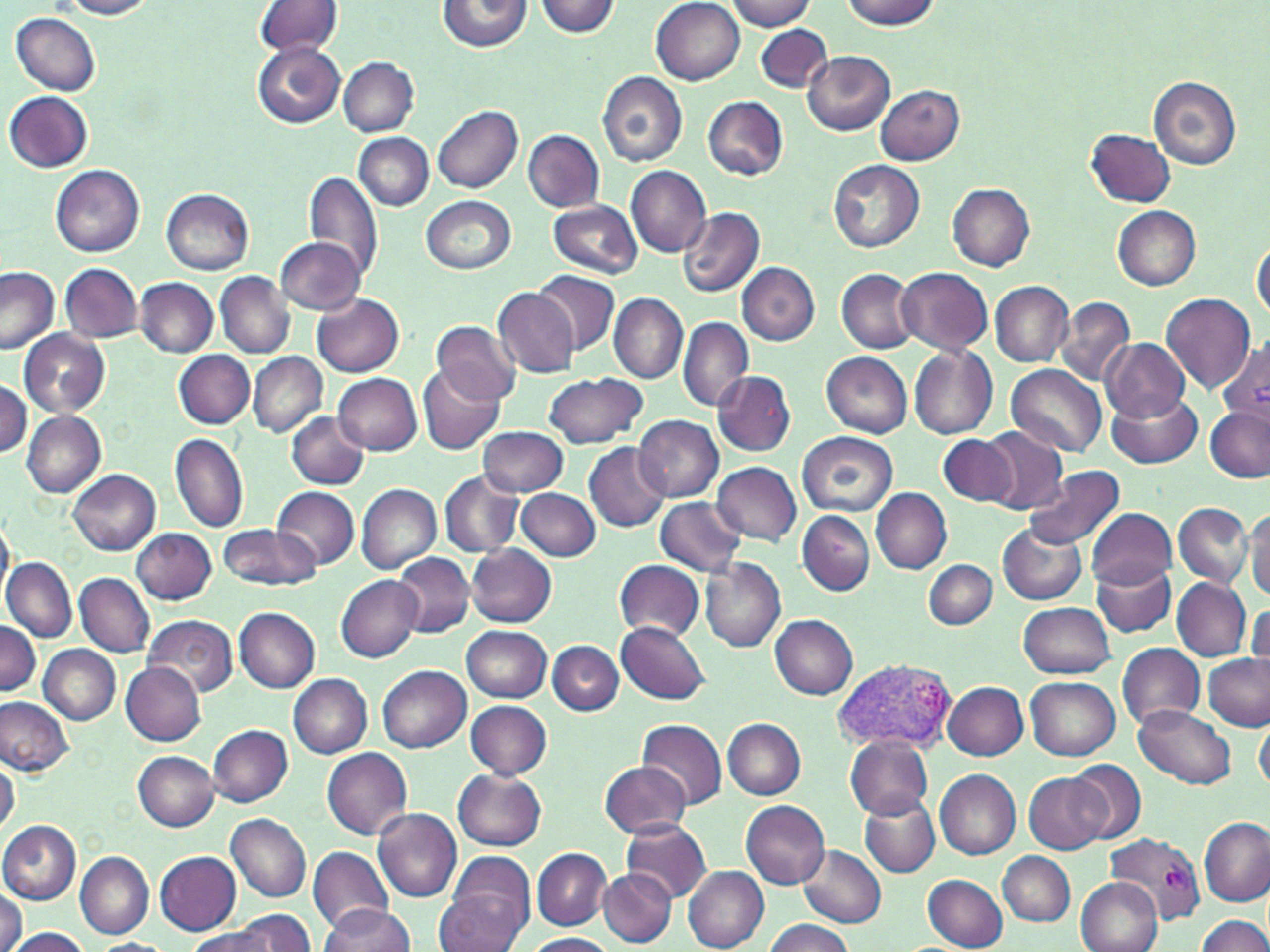

Approximate bounding boxes as (x1, y1, x2, y2) in pixels. Uninfected red blood cell locations: (56, 0, 158, 20), (724, 0, 817, 32), (253, 1, 342, 59), (436, 1, 531, 53), (534, 1, 622, 37), (651, 1, 745, 85), (839, 1, 942, 29), (11, 12, 101, 95), (756, 26, 832, 92), (251, 39, 345, 129), (803, 52, 895, 136), (339, 58, 420, 136), (598, 71, 688, 167), (1149, 76, 1243, 169), (874, 85, 964, 165), (4, 91, 92, 172), (702, 96, 789, 180), (433, 105, 524, 194), (1086, 128, 1175, 208), (523, 130, 603, 211), (353, 133, 433, 210), (828, 160, 924, 253), (51, 165, 145, 258), (626, 166, 711, 258), (306, 172, 384, 284), (948, 184, 1035, 271), (162, 188, 255, 276), (421, 194, 517, 274), (548, 200, 642, 277), (677, 206, 765, 297), (1111, 206, 1201, 290), (276, 237, 366, 315), (1252, 238, 1269, 320), (43, 262, 134, 408), (737, 263, 819, 345), (60, 264, 143, 340), (0, 266, 58, 355), (895, 267, 993, 356), (533, 269, 621, 355), (837, 270, 919, 353), (216, 272, 294, 357), (136, 278, 217, 357), (989, 281, 1073, 366), (493, 289, 578, 377), (608, 293, 688, 383), (1159, 293, 1256, 394), (313, 294, 404, 377), (1055, 297, 1134, 386), (679, 317, 753, 412), (431, 321, 522, 406), (19, 329, 111, 417), (1101, 338, 1190, 421), (1221, 340, 1269, 426), (909, 346, 998, 439), (174, 350, 255, 428), (821, 351, 911, 437), (247, 352, 327, 438), (1006, 363, 1107, 457), (418, 366, 504, 455), (712, 372, 796, 456), (332, 373, 421, 453), (542, 373, 647, 449), (0, 381, 30, 457), (1105, 387, 1201, 469), (1205, 406, 1269, 483), (22, 410, 106, 498), (287, 411, 369, 489), (633, 415, 722, 501), (477, 426, 568, 497), (979, 426, 1069, 515), (796, 431, 898, 518), (171, 432, 248, 534), (939, 434, 1019, 508), (583, 442, 669, 531), (713, 462, 801, 544), (1022, 466, 1124, 551), (69, 470, 160, 556), (438, 471, 524, 558), (356, 484, 442, 574), (271, 486, 358, 570), (871, 487, 952, 573), (517, 488, 600, 562), (654, 497, 747, 576), (1173, 503, 1253, 587), (1244, 504, 1270, 599), (1088, 508, 1178, 588), (1, 510, 14, 604), (796, 511, 873, 595), (996, 523, 1087, 605), (218, 524, 317, 592), (131, 528, 216, 603), (467, 543, 557, 627), (392, 552, 474, 637), (3, 557, 75, 642), (700, 557, 786, 654), (923, 559, 997, 630), (614, 560, 705, 640), (1091, 562, 1177, 637), (75, 573, 155, 656), (337, 575, 421, 662), (1171, 578, 1251, 660), (1248, 599, 1270, 675), (1020, 601, 1116, 678), (233, 606, 319, 692), (769, 614, 859, 700), (140, 615, 237, 699), (0, 622, 41, 695), (616, 622, 711, 703), (462, 625, 552, 702), (547, 641, 623, 715), (1117, 642, 1204, 731), (40, 645, 119, 724), (1202, 653, 1268, 731), (122, 663, 206, 744), (377, 664, 470, 752), (288, 674, 372, 757), (1026, 676, 1120, 760), (943, 681, 1029, 761), (0, 696, 74, 775), (465, 700, 552, 778), (1132, 705, 1237, 790), (1255, 711, 1270, 794), (724, 718, 807, 799), (637, 719, 728, 810), (208, 725, 293, 807), (846, 736, 934, 819), (136, 738, 293, 819), (322, 748, 413, 839), (133, 751, 219, 830), (1, 757, 20, 833), (599, 760, 692, 839), (1067, 760, 1145, 844), (453, 769, 547, 850), (934, 770, 1021, 859), (1026, 773, 1112, 852), (858, 796, 941, 879), (741, 801, 829, 889), (373, 807, 462, 901), (225, 814, 311, 902), (1199, 817, 1268, 906), (0, 820, 81, 905), (620, 820, 712, 902), (309, 845, 392, 931), (797, 845, 887, 929), (532, 848, 611, 930), (154, 851, 242, 935), (998, 851, 1074, 927), (76, 852, 153, 938), (683, 867, 769, 951), (600, 869, 677, 947), (437, 871, 532, 952), (922, 874, 1008, 951), (1074, 877, 1160, 952), (0, 886, 23, 952), (318, 903, 413, 951), (232, 909, 317, 951), (1196, 915, 1270, 952), (763, 919, 854, 952), (6, 927, 93, 951), (185, 927, 277, 952), (521, 933, 616, 951), (88, 939, 174, 952). Plasmodium vivax-infected red blood cell locations: (830, 658, 959, 754), (1105, 832, 1203, 930). Slide-level diagnosis: Plasmodium vivax. Captured at 1000x magnification. Single field of view. Thin blood film. May-Grünwald-Giemsa stain. Image is 1270×952 pixels. Optical microscopy.